Locate and identify every blood parasite.
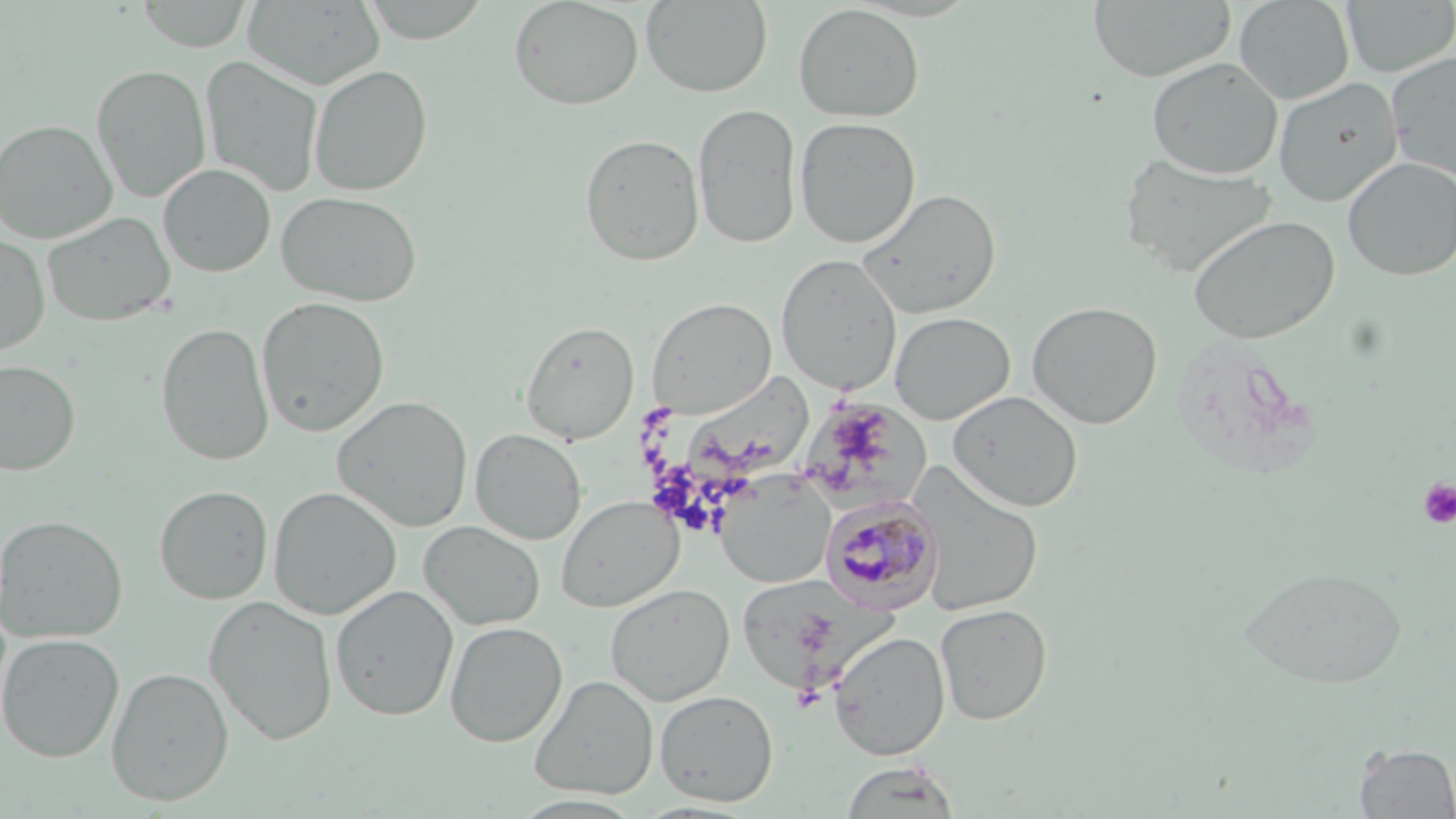

Approximate bounding boxes as [x1, y1, x2, y2] in pixels.
Plasmodium malariae-infected red blood cells: [820, 494, 943, 613].
No Plasmodium falciparum, Plasmodium ovale, Plasmodium vivax, Babesia divergens, or Trypanosoma brucei observed.

Summary:
  - Uninfected red blood cell locations: [136, 0, 254, 51], [357, 0, 494, 43], [509, 0, 644, 110], [1088, 0, 1235, 81], [1234, 0, 1355, 104], [242, 1, 385, 90], [641, 1, 772, 97], [1341, 1, 1456, 77], [793, 4, 924, 122], [1386, 52, 1456, 181], [200, 55, 323, 197], [1147, 57, 1283, 179], [92, 64, 210, 203], [309, 64, 432, 196], [1273, 77, 1403, 206], [693, 102, 802, 248], [794, 116, 921, 249], [0, 118, 117, 243], [579, 133, 704, 266], [1119, 153, 1275, 276], [1342, 156, 1456, 281], [158, 163, 276, 277], [857, 188, 1001, 320], [276, 191, 423, 307], [42, 212, 176, 326], [1188, 215, 1339, 344], [0, 234, 50, 356], [775, 254, 902, 393], [256, 296, 390, 437], [647, 297, 777, 417], [1027, 300, 1163, 429], [889, 311, 1015, 424], [520, 321, 639, 444], [156, 322, 274, 466], [0, 359, 81, 476], [678, 369, 816, 487], [947, 389, 1084, 512], [332, 395, 473, 532], [807, 403, 934, 518], [470, 427, 587, 545], [912, 469, 1045, 616], [714, 474, 835, 588], [154, 485, 273, 604], [267, 486, 402, 620], [557, 495, 683, 611], [1, 513, 128, 643], [419, 520, 545, 630], [1238, 566, 1408, 689], [735, 575, 863, 695], [605, 583, 735, 705], [330, 584, 459, 720], [203, 594, 339, 745], [935, 603, 1052, 725], [445, 621, 567, 747], [829, 631, 950, 761], [0, 633, 124, 763], [106, 666, 233, 806], [529, 674, 659, 799], [654, 690, 779, 806], [1354, 743, 1455, 818], [839, 760, 961, 818], [509, 794, 647, 817]
  - Platelet locations: [1417, 479, 1456, 529]
  - Slide-level diagnosis: Plasmodium malariae
  - Stain: May-Grünwald-Giemsa
  - Preparation: thin blood film
  - Modality: optical microscopy
  - Magnification: 1000x
  - Field of view: single
  - Image size: 1456×819 pixels